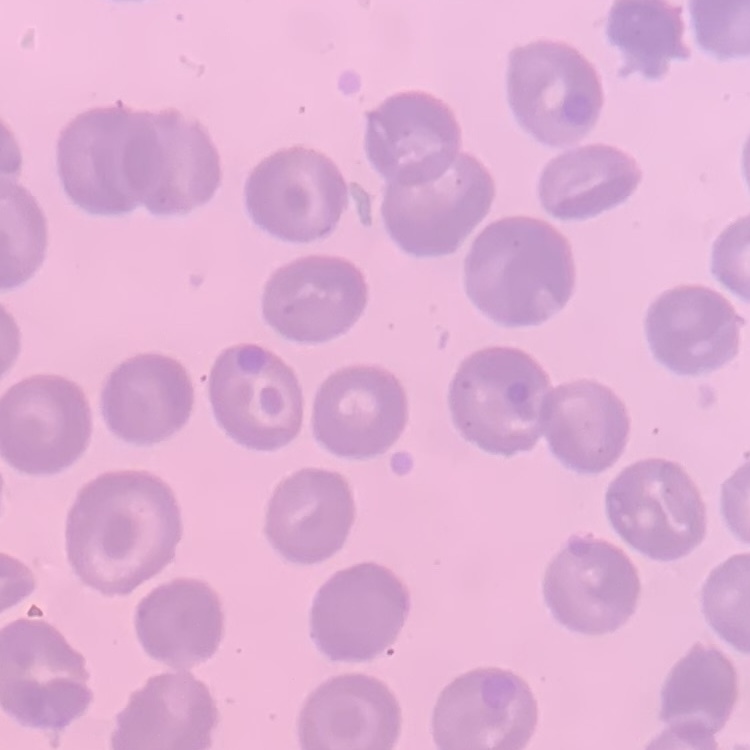

{
  "red_blood_cell_morphology": "no rouleaux formation",
  "preparation": "thin blood film",
  "stain": "Field's or Giemsa",
  "image_type": "one tile cut from a larger photomicrograph"
}